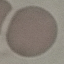
malaria status = uninfected
preparation = thin smear
capture = smartphone camera at the microscope eyepiece
stain = Giemsa
image type = cell patch, automatically extracted from a larger field of view and resized to 64 × 64 pixels